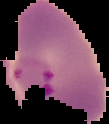

The area outside the segmented cell region is set to black. Image is 109×124 pixels. Malaria status: parasitized. From a thin blood film.